Report the malaria status of this cell.
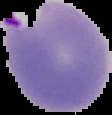
Parasitized.

Cell region segmented out of the field of view; the surrounding area is masked to black. From a thin blood film. Image is 112×115 pixels.